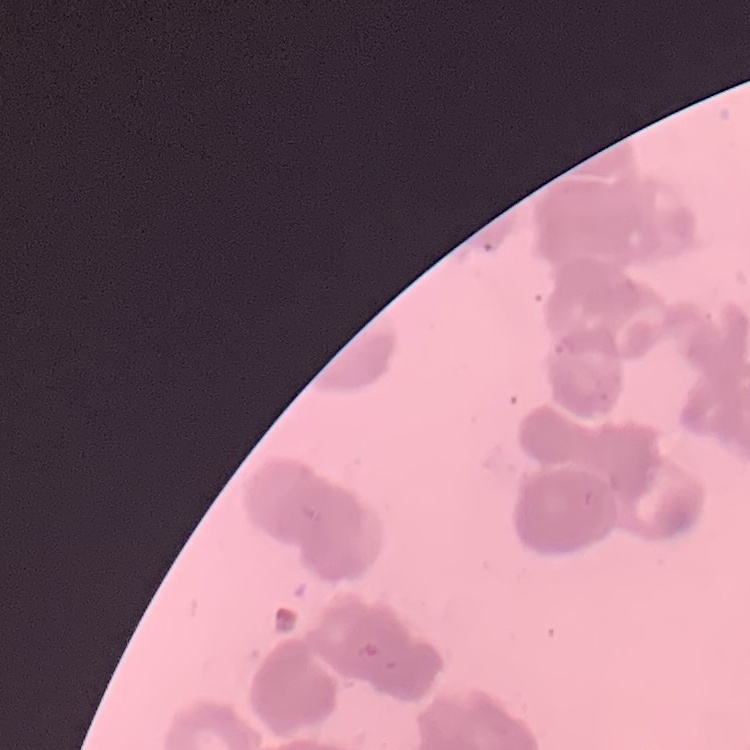 The erythrocytes exhibit rouleaux formation. One tile cut from a larger photomicrograph. Stained with either Field's or Giemsa. Thin blood film.